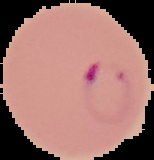

image_type: segmented cell region with the area outside set to black
result: Plasmodium parasites detected
image_size: 154×160 pixels
preparation: thin blood film